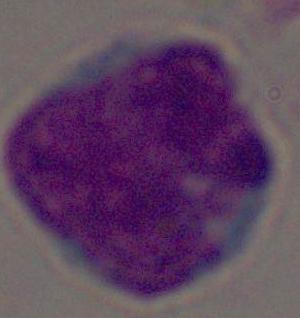
Photomicrograph. A white blood cell is shown. Captured at 1000x magnification.